Classify this cell by malaria status.
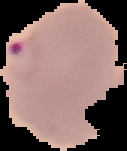

Parasitized.

preparation = thin blood film
image size = 127×151 pixels
image type = segmented cell region with the area outside set to black